Assess this cell for malaria.
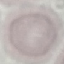
It is uninfected.

Summary:
  - Capture: smartphone through the microscope eyepiece
  - Image type: automatically extracted cell patch, resized to 64 × 64 pixels
  - Preparation: thin blood smear
  - Stain: Giemsa